Classify this cell by malaria status.
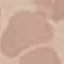
It is uninfected.

Summary:
  - Preparation: thin blood smear
  - Stain: Giemsa
  - Capture: smartphone through the microscope eyepiece
  - Image type: automatically extracted cell patch, resized to 64 × 64 pixels